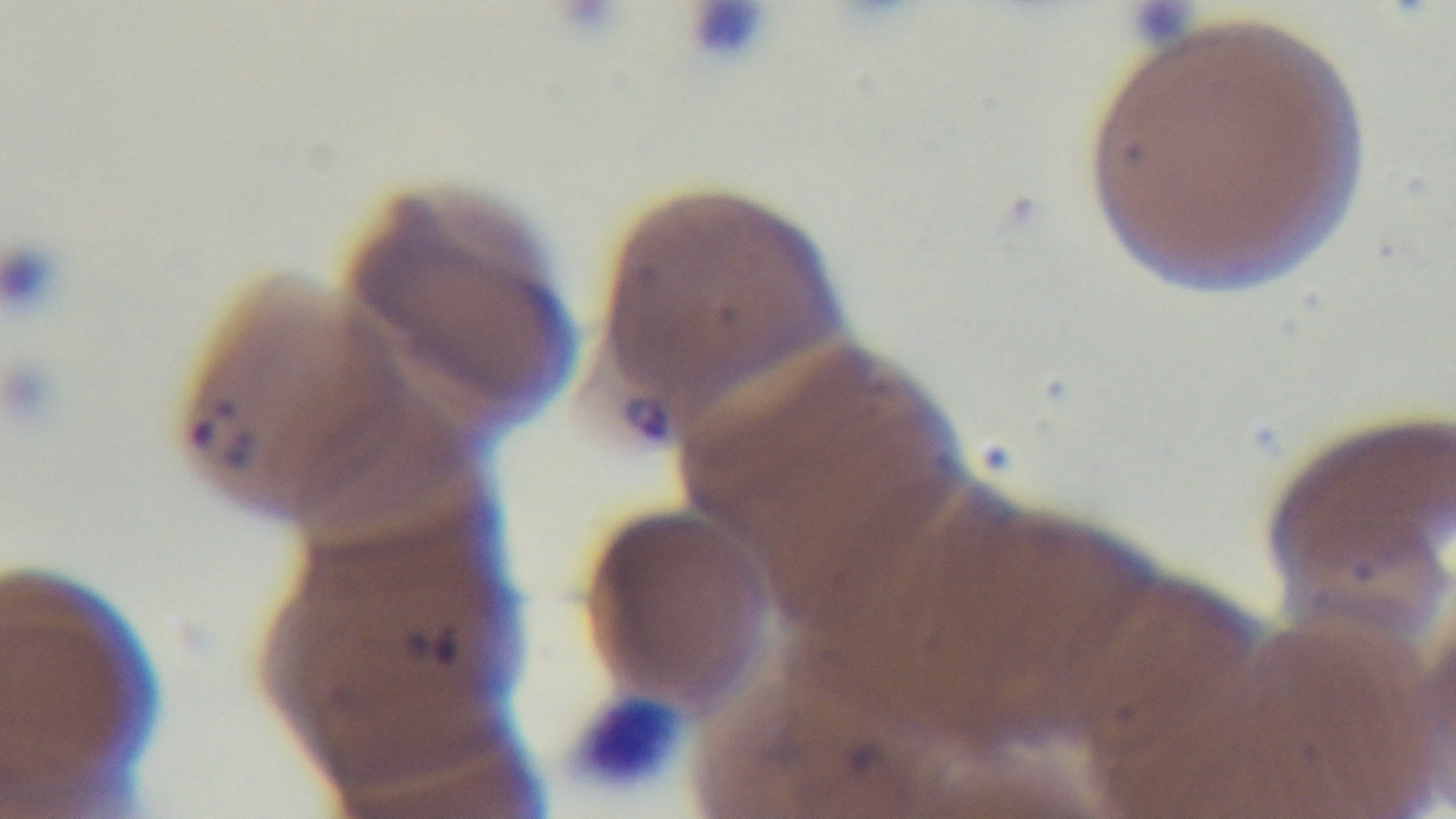 Mounted 4K digital camera. Giemsa-stained. Malaria status: positive. Photomicrograph. Single field of view. Oil-immersion objective, 100x. Preparation: thin smear.